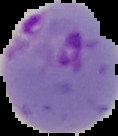
Image is 118×136 pixels. Malaria status: parasitized. From a thin blood film. Cell region segmented out of the field of view; the surrounding area is masked to black.